Outline each Plasmodium ovale-infected red blood cell.
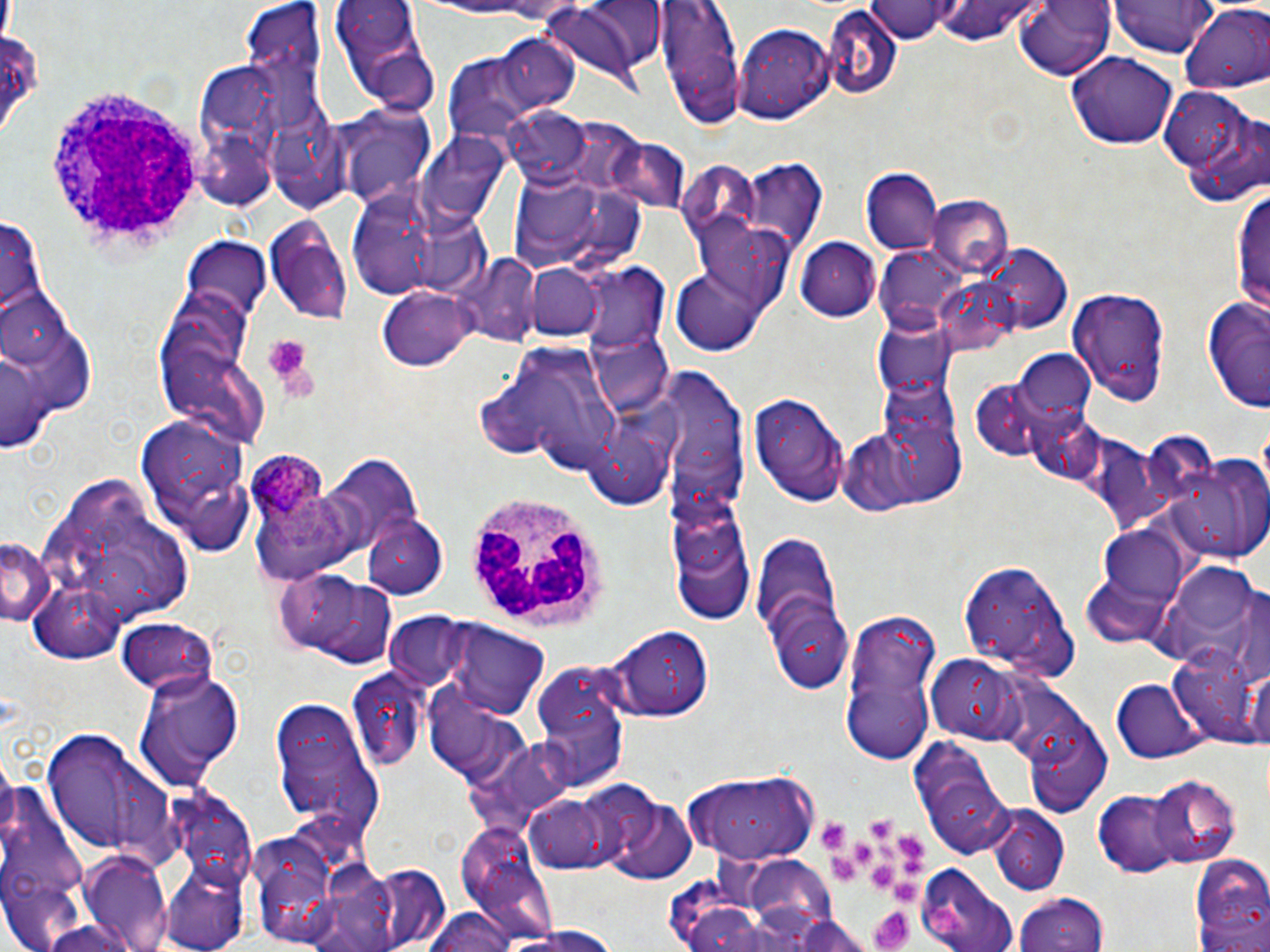
Approximate bounding boxes as (x1, y1, x2, y2) in pixels.
Plasmodium ovale-infected red blood cells: (248, 452, 343, 553).

Platelet locations: (261, 333, 312, 383), (871, 816, 894, 842), (823, 823, 846, 850), (898, 833, 923, 860), (854, 842, 877, 865), (878, 845, 897, 863), (832, 857, 855, 883), (901, 860, 927, 875), (872, 864, 895, 887), (892, 882, 916, 904), (870, 908, 915, 952). Uninfected red blood cell locations: (654, 0, 747, 129), (1017, 0, 1117, 79), (1114, 0, 1215, 58), (327, 1, 438, 114), (869, 1, 962, 44), (927, 1, 1039, 48), (244, 3, 328, 104), (541, 4, 651, 88), (1181, 7, 1269, 92), (823, 10, 902, 99), (736, 24, 836, 124), (494, 35, 581, 116), (1070, 50, 1178, 148), (442, 55, 535, 145), (1160, 85, 1268, 209), (338, 105, 436, 208), (502, 108, 591, 186), (419, 132, 510, 227), (741, 157, 828, 258), (862, 169, 942, 258), (507, 170, 640, 272), (346, 183, 487, 303), (1236, 185, 1270, 321), (929, 194, 1014, 278), (264, 214, 354, 325), (0, 215, 48, 326), (794, 236, 880, 321), (181, 239, 274, 320), (983, 245, 1069, 331), (455, 254, 539, 345), (523, 261, 603, 339), (581, 266, 671, 359), (673, 266, 768, 354), (377, 286, 474, 372), (0, 290, 75, 369), (1068, 290, 1171, 406), (1202, 293, 1270, 417), (870, 320, 958, 399), (587, 328, 674, 421), (488, 342, 626, 472), (1, 347, 49, 451), (1016, 348, 1095, 430), (654, 366, 746, 507), (969, 378, 1051, 458), (751, 387, 850, 504), (134, 415, 252, 556), (1173, 450, 1270, 560), (317, 452, 423, 558), (36, 468, 199, 637), (666, 491, 752, 619), (361, 514, 449, 600), (1099, 527, 1192, 606), (751, 531, 846, 660), (0, 537, 52, 625), (957, 555, 1078, 682), (1161, 560, 1263, 658), (292, 576, 400, 668), (766, 594, 855, 692), (837, 608, 941, 760), (383, 613, 466, 688), (114, 615, 218, 697), (446, 620, 550, 716), (612, 626, 712, 723), (1168, 644, 1265, 744), (927, 653, 1024, 742), (1246, 663, 1269, 756), (529, 666, 629, 791), (133, 668, 246, 792), (345, 671, 429, 770), (1112, 676, 1205, 764), (270, 698, 384, 832), (1023, 724, 1114, 816), (38, 728, 178, 860), (911, 745, 1016, 862), (679, 769, 823, 864), (1148, 775, 1239, 869), (600, 790, 698, 882), (1094, 790, 1186, 876), (524, 794, 623, 876), (988, 810, 1068, 894), (455, 823, 558, 940), (243, 826, 353, 947), (82, 850, 172, 952), (1188, 851, 1270, 948), (739, 856, 837, 939), (357, 862, 451, 952), (917, 862, 1021, 952), (304, 864, 414, 952), (1014, 893, 1108, 952), (422, 909, 519, 952), (765, 909, 879, 952), (492, 924, 625, 951). White blood cell locations: (43, 80, 210, 258), (466, 491, 609, 628). Slide-level diagnosis: Plasmodium ovale. Image is 1270×952 pixels. Captured at 1000x magnification. Thin blood smear. May-Grünwald-Giemsa-stained preparation. One field of a larger specimen. Light microscopy.